Name the parasite shown.
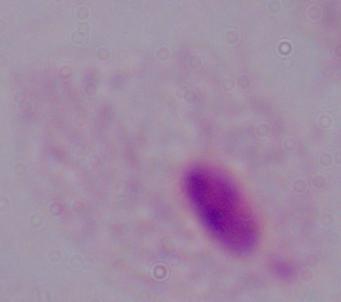

A trichomonad.

magnification = 1000x
modality = photomicrograph